Locate every leukocyte (white blood cell).
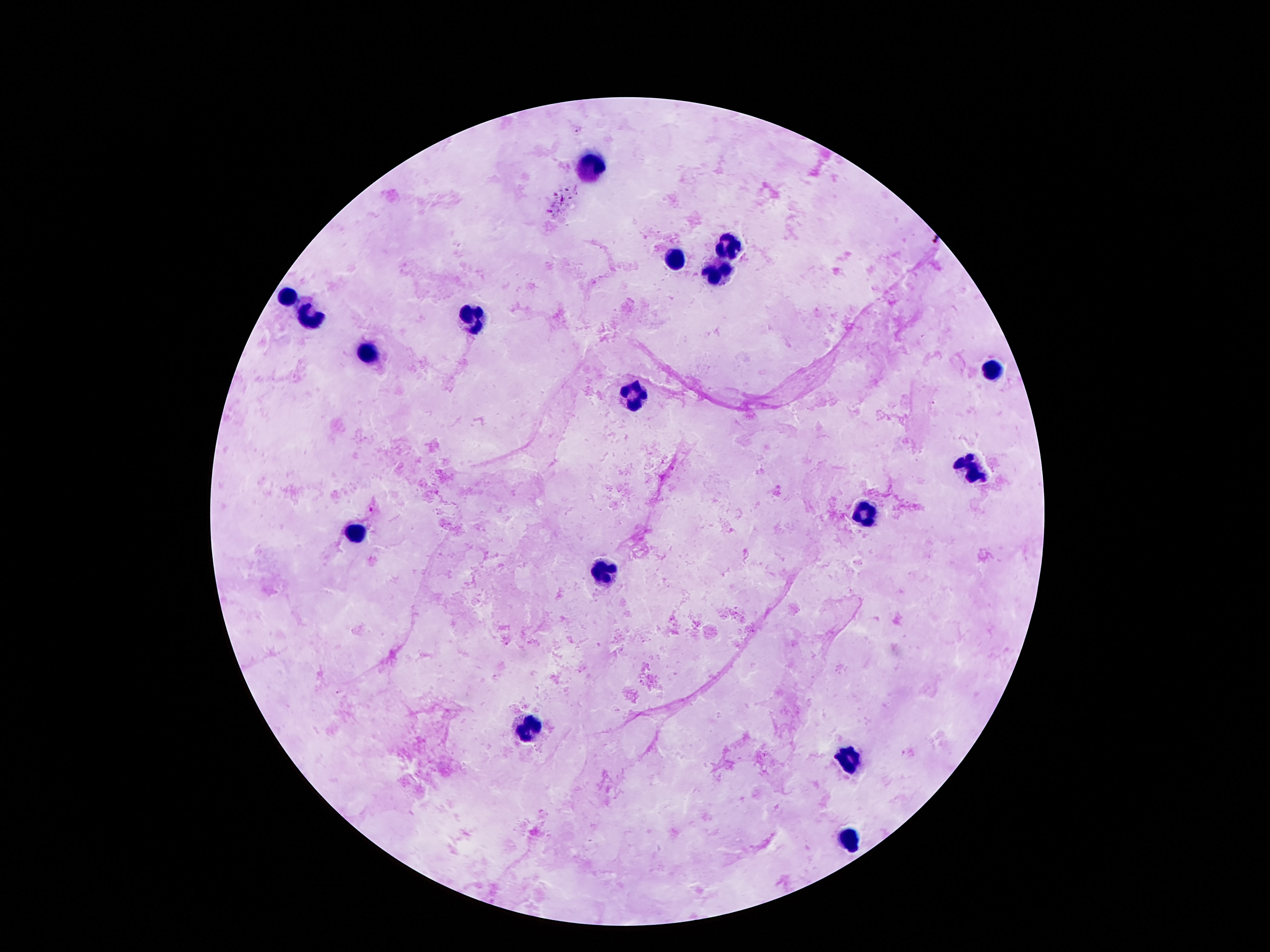

Approximate centers as {x, y} in pixels.
Leukocytes: {589, 166}, {730, 247}, {675, 258}, {718, 271}, {286, 298}, {474, 314}, {311, 318}, {372, 355}, {991, 369}, {634, 397}, {970, 469}, {866, 514}, {354, 533}, {603, 574}, {526, 727}, {847, 758}, {849, 840}.

Summary:
  - Preparation: thick blood smear
  - Patient malaria status: negative
  - Magnification: 100x
  - Capture: smartphone camera through the microscope eyepiece
  - Stain: Giemsa
  - Field of view: single
  - Image size: 1270×952 pixels